Assess for Plasmodium parasites.
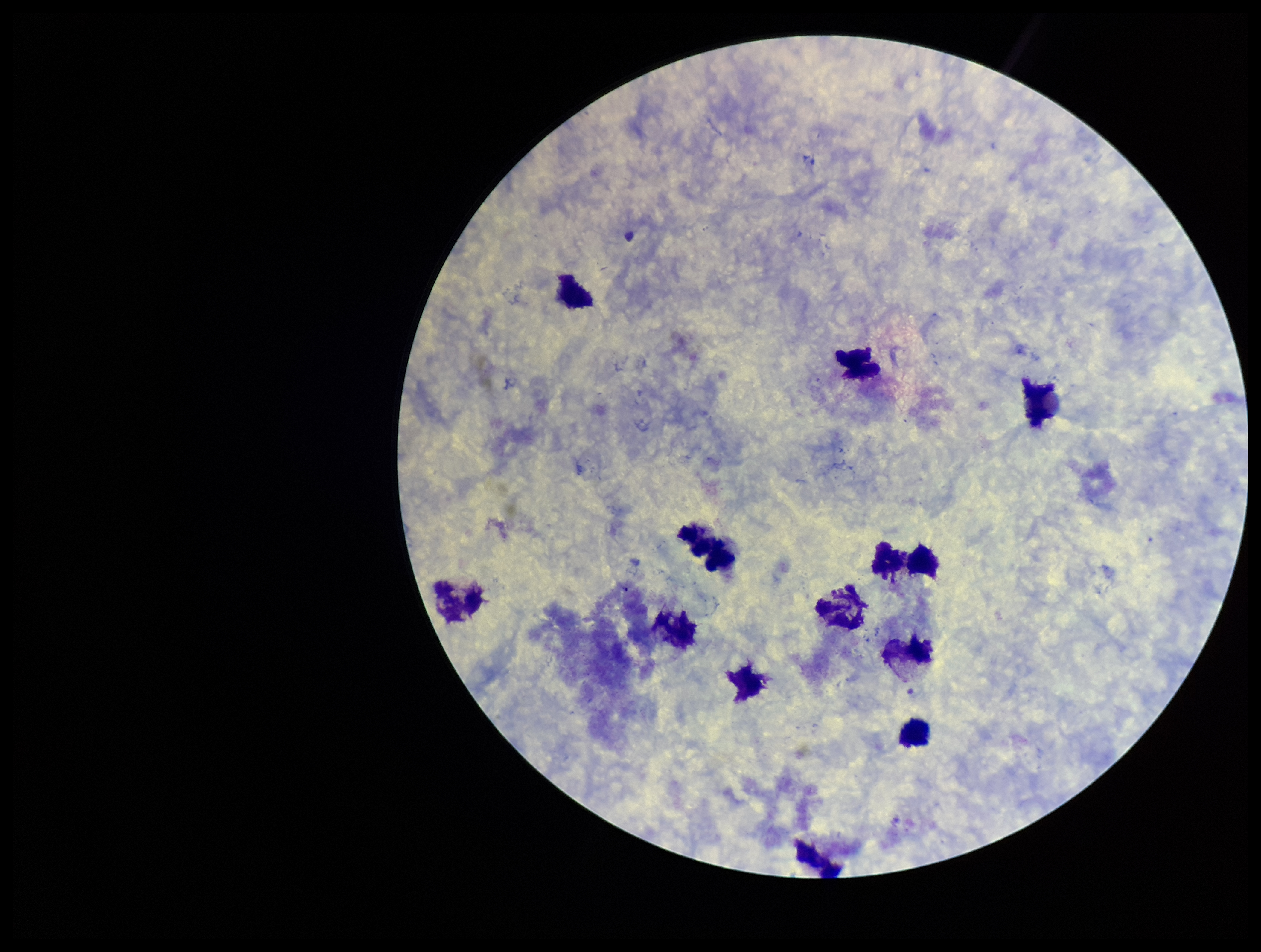

None identified.

preparation = thick blood smear
parasite count = 0
field of view = one from this slide
patient malaria status = negative
capture = smartphone photograph through the microscope eyepiece
leukocyte count = 13
image size = 1261×952 pixels
stain = Giemsa